Assess this cell for malaria.
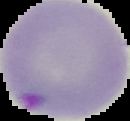
Parasitized.

Summary:
  - Image type: segmented cell region on a black background
  - Preparation: thin blood smear
  - Image size: 130×121 pixels